State the blood parasite species.
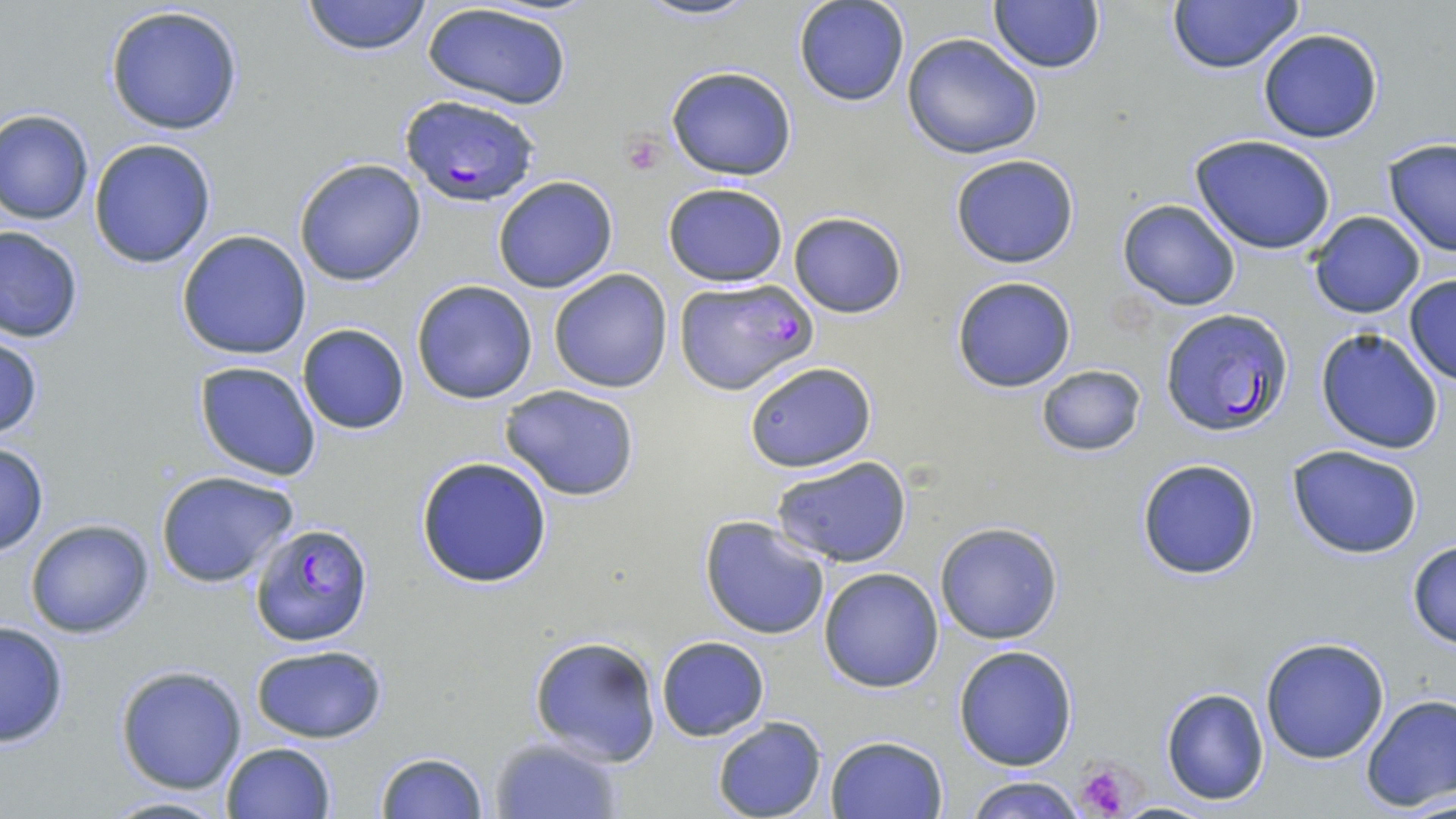

Plasmodium falciparum.

Approximate bounding boxes as (x1,y1)-(x2,y2) corner pairs in pixels. Platelet locations: (622,135)-(665,176), (1074,759)-(1140,819). Plasmodium falciparum-infected red blood cell locations: (398,92)-(541,206), (672,276)-(817,393), (1160,308)-(1294,435), (250,522)-(375,647). Uninfected red blood cell locations: (300,0)-(433,56), (635,0)-(757,23), (1167,0)-(1304,73), (792,1)-(909,107), (988,1)-(1106,73), (421,2)-(574,111), (103,4)-(245,136), (1257,27)-(1384,143), (900,34)-(1042,160), (665,64)-(799,181), (0,109)-(95,226), (1189,134)-(1339,257), (88,137)-(218,269), (1382,139)-(1456,257), (949,152)-(1081,269), (293,158)-(426,285), (492,175)-(619,294), (663,181)-(790,287), (1117,200)-(1240,310), (788,211)-(907,318), (1306,211)-(1426,318), (0,225)-(84,344), (176,231)-(311,360), (547,269)-(672,393), (1403,274)-(1456,384), (951,275)-(1077,393), (411,279)-(539,404), (296,323)-(411,435), (0,329)-(45,442), (1315,329)-(1445,455), (741,359)-(877,472), (193,361)-(323,482), (1035,364)-(1146,457), (499,384)-(642,501), (0,440)-(48,557), (1285,444)-(1426,561), (415,456)-(554,588), (771,456)-(915,569), (1135,457)-(1262,580), (154,470)-(301,589), (699,514)-(832,640), (25,519)-(153,638), (936,522)-(1063,644), (1406,540)-(1456,651), (818,566)-(945,693), (0,621)-(71,748), (528,636)-(662,766), (656,636)-(771,742), (1259,636)-(1391,762), (248,644)-(388,744), (953,644)-(1078,771), (115,664)-(248,794), (1160,687)-(1269,805), (1360,693)-(1456,813), (712,715)-(828,819), (825,734)-(948,818), (489,735)-(624,818), (220,741)-(337,819), (375,750)-(489,818), (962,775)-(1094,819), (100,795)-(231,818). Light microscopy. Image is 1456×819 pixels. Captured at 1000x magnification. Thin blood smear. May-Grünwald-Giemsa stain. One field of a larger specimen.